Outline each blood parasite and name the species.
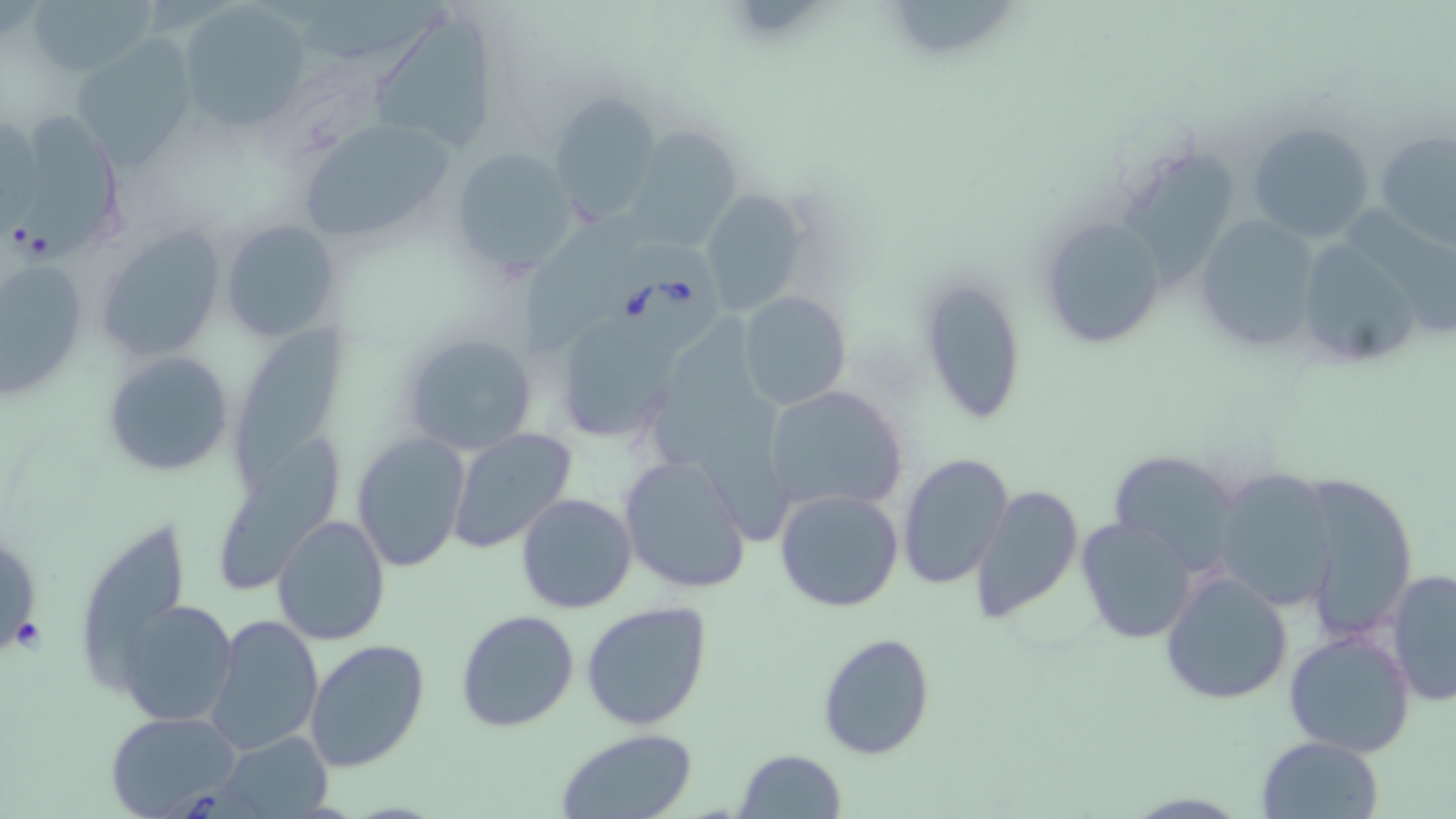

Approximate bounding boxes as (x1, y1, x2, y2) in pixels.
Babesia divergens-infected red blood cells: (605, 230, 725, 354).
No Plasmodium falciparum, Plasmodium ovale, Plasmodium malariae, Plasmodium vivax, or Trypanosoma brucei observed.

Uninfected red blood cell locations: (896, 0, 1019, 62), (28, 1, 156, 79), (279, 1, 460, 60), (177, 5, 308, 131), (373, 21, 503, 151), (69, 39, 195, 167), (547, 91, 662, 229), (8, 108, 129, 261), (296, 120, 456, 240), (1247, 121, 1376, 242), (624, 127, 743, 248), (1375, 130, 1456, 246), (448, 146, 582, 277), (1126, 153, 1246, 286), (696, 186, 810, 318), (1345, 202, 1456, 334), (1035, 209, 1175, 349), (1191, 213, 1325, 352), (220, 218, 338, 344), (529, 218, 635, 353), (96, 226, 228, 361), (1307, 246, 1416, 357), (1, 247, 87, 402), (917, 275, 1027, 427), (737, 292, 850, 410), (656, 309, 763, 466), (568, 321, 675, 440), (233, 324, 354, 494), (398, 332, 538, 458), (103, 351, 235, 478), (763, 384, 910, 515), (701, 398, 796, 549), (449, 429, 575, 555), (220, 432, 342, 597), (353, 432, 470, 572), (1106, 451, 1245, 569), (898, 454, 1015, 590), (618, 455, 752, 595), (1212, 466, 1342, 609), (1301, 474, 1420, 638), (971, 484, 1084, 622), (774, 488, 905, 613), (515, 491, 638, 614), (273, 514, 390, 645), (1076, 516, 1199, 642), (89, 522, 187, 693), (0, 550, 34, 654), (1159, 567, 1294, 706), (1384, 568, 1455, 706), (115, 598, 239, 728), (580, 601, 713, 732), (456, 609, 580, 732), (204, 614, 323, 756), (1284, 628, 1417, 757), (817, 630, 935, 759), (304, 638, 431, 773), (105, 710, 243, 817), (555, 728, 702, 819), (217, 732, 334, 817), (1256, 736, 1386, 819), (736, 749, 847, 819). Slide-level diagnosis: Babesia divergens. One field of a larger specimen. Image is 1456×819 pixels. Thin blood film. Optical microscopy. Captured at 1000x magnification. May-Grünwald-Giemsa-stained preparation.